Locate and identify every blood parasite.
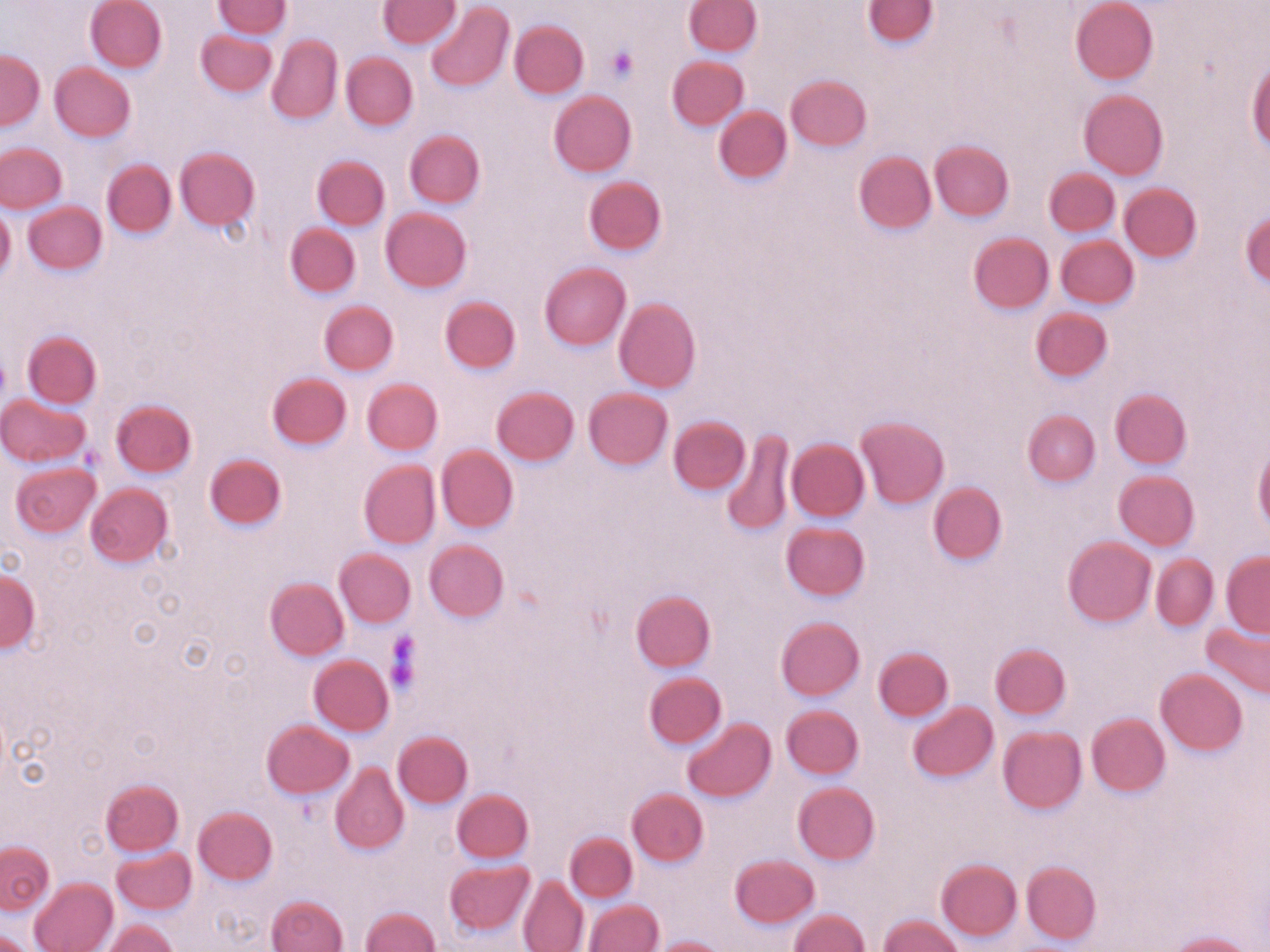

No blood parasites observed.

{
  "slide_level_diagnosis": "negative for blood parasites",
  "image_size": "1270×952 pixels",
  "modality": "light microscopy",
  "preparation": "thin blood film",
  "uninfected_red_blood_cell_locations": "approximate bounding boxes as (x1, y1, x2, y2) in pixels: (85, 0, 166, 73), (214, 0, 290, 38), (379, 0, 458, 48), (864, 0, 937, 48), (1071, 0, 1158, 85), (425, 1, 514, 93), (684, 1, 762, 57), (510, 20, 589, 99), (196, 29, 278, 97), (267, 34, 343, 125), (271, 42, 417, 125), (0, 49, 45, 129), (341, 52, 417, 130), (667, 55, 749, 130), (1248, 58, 1268, 156), (50, 63, 135, 142), (785, 75, 871, 152), (548, 90, 636, 177), (1079, 90, 1168, 180), (714, 107, 792, 183), (405, 130, 484, 209), (931, 140, 1014, 221), (0, 143, 66, 213), (175, 147, 259, 230), (853, 151, 936, 236), (313, 155, 390, 231), (102, 159, 176, 238), (1045, 168, 1119, 236), (583, 176, 667, 256), (1119, 182, 1203, 262), (23, 201, 107, 275), (0, 204, 15, 280), (379, 207, 472, 293), (1241, 211, 1270, 287), (285, 222, 361, 298), (968, 233, 1053, 314), (1056, 236, 1139, 309), (538, 263, 630, 351), (440, 296, 521, 375), (613, 298, 700, 394), (319, 301, 398, 376), (1030, 307, 1113, 382), (22, 330, 102, 408), (266, 372, 351, 451), (362, 378, 443, 456), (491, 385, 579, 466), (583, 387, 673, 470), (1110, 388, 1192, 469), (0, 394, 90, 467), (111, 399, 196, 478), (1022, 410, 1100, 486), (669, 416, 750, 495), (857, 416, 949, 509), (722, 428, 795, 538), (787, 439, 869, 521), (1254, 442, 1270, 536), (436, 445, 518, 533), (203, 453, 287, 531), (359, 459, 441, 549), (10, 462, 101, 539), (1113, 471, 1199, 550), (928, 481, 1007, 566), (85, 483, 173, 569), (782, 522, 870, 601), (1062, 537, 1155, 627), (423, 540, 508, 623), (334, 549, 415, 628), (1221, 551, 1270, 637), (1152, 553, 1219, 631), (1, 568, 39, 653), (265, 576, 349, 661), (631, 589, 716, 672), (776, 617, 864, 701), (1202, 620, 1270, 700), (990, 643, 1070, 721), (873, 646, 954, 722), (309, 655, 396, 736), (1156, 669, 1248, 755), (645, 672, 727, 749), (908, 701, 997, 783), (781, 704, 863, 779), (1086, 713, 1171, 797), (682, 718, 775, 802), (261, 719, 353, 798), (997, 726, 1086, 814), (393, 731, 473, 807), (330, 760, 409, 855), (100, 779, 184, 856), (792, 781, 880, 865), (452, 788, 534, 863), (627, 789, 708, 867), (192, 807, 277, 885), (565, 832, 637, 902), (1, 840, 54, 914), (111, 847, 195, 915), (731, 853, 819, 928), (935, 859, 1021, 941), (445, 860, 534, 936), (1022, 861, 1100, 945), (517, 875, 589, 952), (29, 876, 117, 952), (267, 895, 348, 952), (584, 900, 663, 952), (361, 905, 441, 952), (788, 908, 870, 951), (879, 915, 963, 952), (100, 918, 179, 952), (0, 928, 40, 952), (1166, 931, 1255, 952), (652, 935, 727, 952)",
  "magnification": "1000x",
  "field_of_view": "single",
  "platelet_locations": "approximate bounding boxes as (x1, y1, x2, y2) in pixels: (606, 45, 638, 82), (0, 355, 9, 399), (385, 633, 421, 694)",
  "stain": "May-Grünwald-Giemsa"
}